Report the malaria status of this cell.
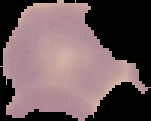
It is uninfected.

Image is 151×121 pixels. The area outside the segmented cell region is set to black. From a thin blood smear.